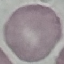

malaria status = uninfected
image type = cell patch, automatically extracted from a larger field of view and resized to 64 × 64 pixels
preparation = thin blood film
capture = smartphone through the microscope eyepiece
stain = Giemsa